Assess this cell for malaria.
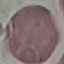

Uninfected.

Summary:
  - Stain: Giemsa
  - Capture: smartphone through the microscope eyepiece
  - Preparation: thin blood smear
  - Image type: cell patch, automatically extracted from a larger field of view and resized to 64 × 64 pixels